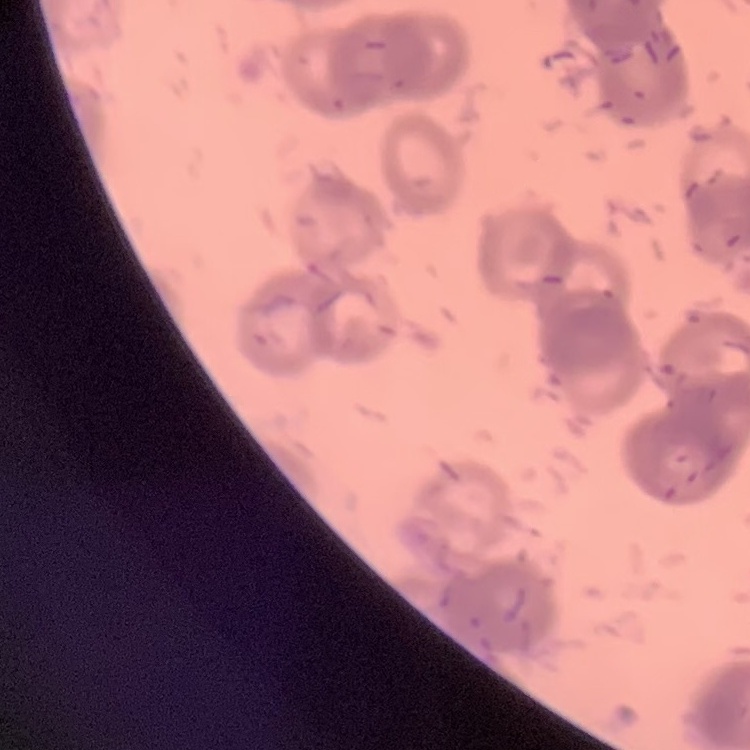
Summary:
  - Red blood cell morphology: rouleaux formation
  - Stain: Field's or Giemsa
  - Image type: one tile cut from a larger photomicrograph
  - Preparation: thin peripheral smear